Assess this cell for malaria.
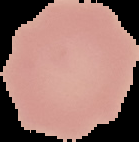

It is uninfected.

image size = 139×142 pixels
preparation = thin blood film
image type = segmented cell region with the area outside set to black